Locate every parasitized red blood cell.
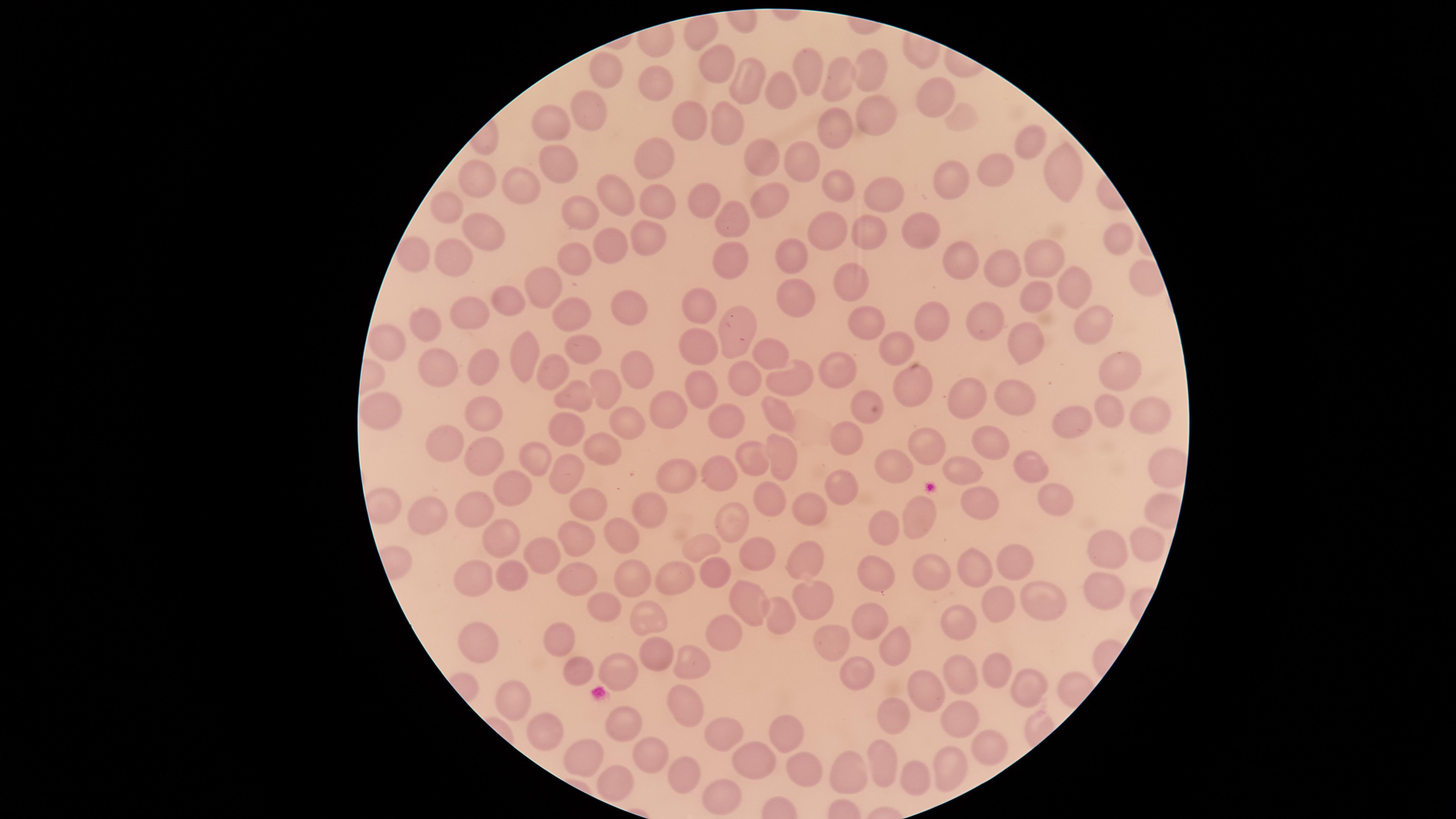
No parasitized red blood cells identified.

Approximate marker points as (x, y) in pixels.
Summary:
  - Uninfected red blood cells: (694, 23), (868, 66), (716, 68), (804, 70), (606, 72), (836, 76), (748, 78), (659, 80), (777, 92), (930, 92), (877, 107), (590, 109), (684, 115), (965, 119), (549, 121), (722, 121), (835, 125), (1029, 131), (553, 152), (760, 152), (655, 154), (799, 159), (992, 170), (1068, 173), (479, 178), (519, 180), (838, 182), (608, 186), (949, 187), (882, 188), (768, 194), (702, 197), (440, 199), (656, 201), (585, 214), (734, 220), (917, 227), (489, 230), (824, 231), (864, 232), (1113, 235), (608, 237), (646, 240), (458, 251), (412, 252), (785, 256), (960, 257), (1041, 258), (736, 259), (574, 260), (1009, 270), (849, 274), (540, 283), (1070, 285), (791, 293), (1035, 299), (512, 301), (702, 305), (627, 307), (466, 312), (566, 313), (858, 318), (934, 318), (1089, 318), (428, 322), (987, 323), (730, 333), (1027, 340), (388, 342), (900, 342), (585, 344), (702, 344), (526, 350), (768, 350), (440, 363), (487, 363), (637, 366), (835, 366), (553, 370), (1120, 370), (742, 377), (794, 379), (605, 382), (911, 384), (703, 388), (575, 395), (860, 395), (967, 395), (1016, 397), (486, 405), (668, 405), (1111, 407), (1148, 407), (382, 409), (780, 413), (632, 416), (725, 416), (1072, 422), (575, 424), (841, 434), (928, 441), (600, 442), (448, 443), (988, 445), (780, 452), (754, 454), (487, 457), (538, 458), (898, 464), (961, 465), (1033, 465), (566, 468), (718, 471), (673, 476), (840, 485), (514, 490), (763, 491), (1055, 496), (972, 497), (583, 499), (648, 505), (480, 508), (916, 509), (423, 511), (813, 512), (724, 518), (882, 527), (577, 534), (507, 535), (632, 535), (1138, 539), (704, 543), (1106, 545), (548, 550), (756, 550), (807, 557), (1020, 563), (713, 566), (925, 569), (975, 570), (629, 571), (576, 574), (669, 574), (879, 576), (517, 578), (477, 581), (1106, 587), (751, 599), (992, 600), (814, 601), (1039, 605), (604, 607), (647, 613), (785, 615), (876, 617), (962, 623), (722, 630), (558, 638), (474, 643), (829, 645), (886, 645), (659, 651), (691, 661), (577, 663), (995, 665), (618, 666), (856, 674), (960, 674), (920, 681), (1027, 681), (507, 690), (682, 700), (894, 718), (958, 718), (617, 724), (784, 727), (718, 728), (550, 736), (983, 747), (652, 752), (881, 759), (751, 760), (586, 761), (803, 762), (852, 768), (683, 771), (950, 771), (909, 774), (616, 783), (719, 792)
  - Field of view: single
  - Preparation: thin smear of blood
  - Capture: smartphone photograph through the microscope eyepiece
  - Image size: 1456×819 pixels
  - Stain: Giemsa
  - Visible region: circular